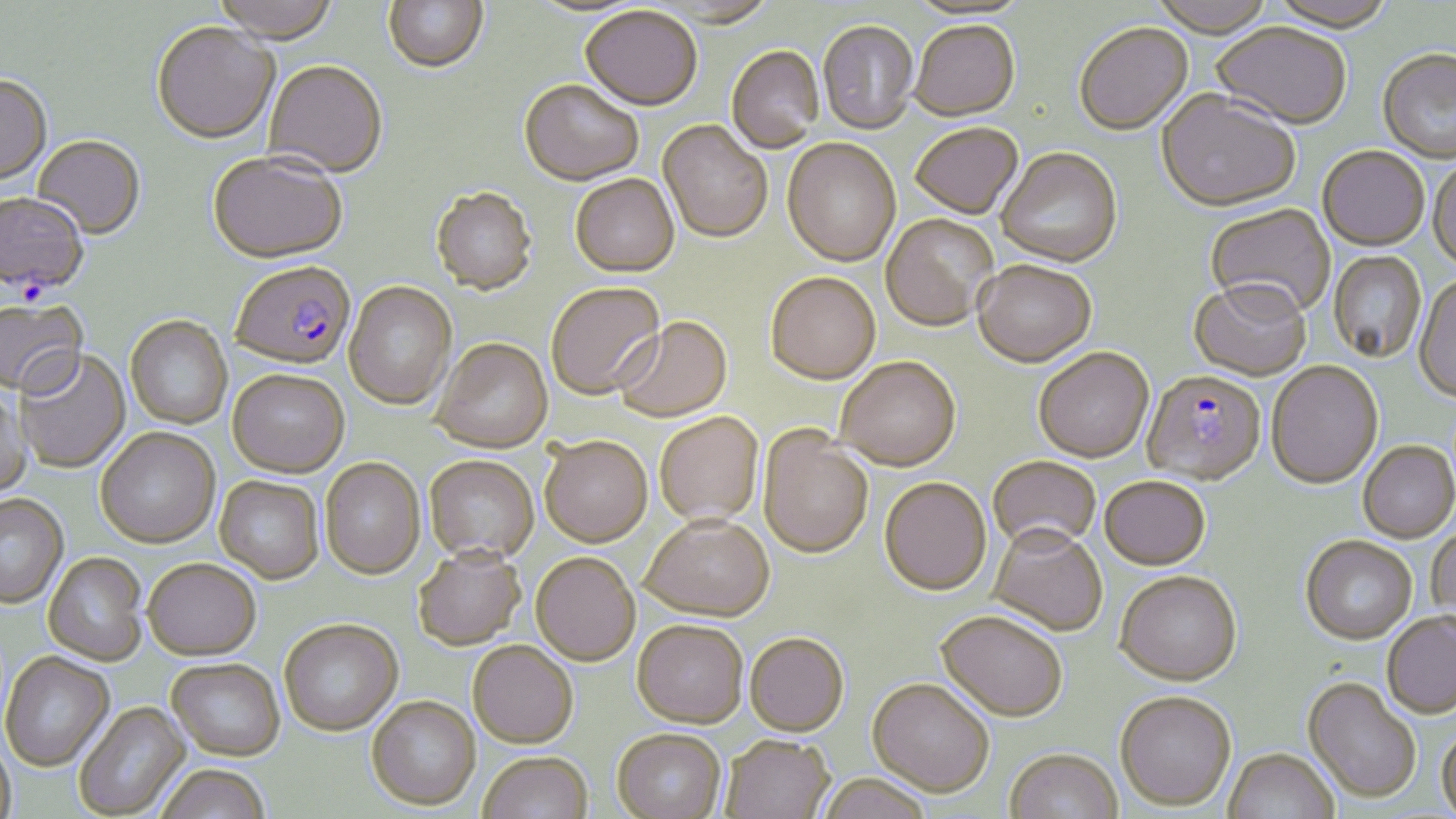

slide-level diagnosis = Plasmodium falciparum
modality = light microscopy
Plasmodium falciparum-infected red blood cell locations = approximate bounding boxes as [x1, y1, x2, y2] in pixels: [0, 194, 89, 298], [229, 263, 355, 374], [1142, 373, 1266, 488]
field of view = single
uninfected red blood cell locations = approximate bounding boxes as [x1, y1, x2, y2] in pixels: [211, 0, 340, 47], [383, 0, 488, 76], [526, 0, 644, 19], [1147, 0, 1277, 41], [1268, 0, 1397, 35], [580, 8, 702, 114], [818, 22, 919, 137], [910, 23, 1020, 124], [151, 24, 279, 148], [1074, 25, 1194, 137], [1211, 25, 1351, 132], [726, 47, 824, 154], [1378, 51, 1456, 165], [263, 63, 387, 180], [0, 77, 53, 188], [519, 81, 643, 189], [1156, 93, 1300, 215], [658, 121, 773, 246], [911, 125, 1023, 221], [32, 137, 145, 241], [782, 140, 900, 268], [1318, 148, 1429, 253], [996, 150, 1123, 270], [208, 155, 348, 267], [1428, 160, 1456, 274], [570, 177, 680, 280], [431, 189, 537, 298], [1205, 204, 1336, 323], [881, 215, 998, 334], [1329, 252, 1426, 364], [972, 264, 1096, 370], [766, 275, 881, 387], [1413, 277, 1456, 405], [343, 282, 457, 411], [1188, 283, 1311, 384], [547, 284, 666, 402], [0, 299, 89, 402], [125, 317, 232, 430], [614, 319, 733, 424], [431, 340, 553, 456], [1034, 349, 1154, 465], [14, 351, 133, 476], [836, 360, 961, 474], [1266, 364, 1383, 492], [227, 372, 349, 481], [0, 388, 33, 499], [655, 414, 764, 528], [757, 429, 873, 561], [95, 430, 220, 551], [539, 439, 653, 550], [1358, 444, 1456, 545], [424, 457, 539, 565], [988, 458, 1100, 557], [320, 460, 425, 582], [214, 477, 324, 586], [880, 480, 991, 598], [1099, 480, 1210, 573], [0, 496, 69, 610], [641, 519, 775, 626], [1427, 526, 1456, 634], [988, 529, 1107, 638], [1300, 538, 1417, 647], [413, 551, 526, 653], [43, 553, 148, 667], [531, 555, 640, 668], [143, 561, 261, 664], [1115, 574, 1242, 690], [935, 614, 1067, 726], [1381, 614, 1456, 721], [279, 622, 403, 738], [632, 624, 748, 731], [745, 636, 849, 739], [468, 643, 577, 751], [1, 653, 115, 772], [166, 660, 285, 764], [1302, 680, 1420, 805], [867, 681, 993, 800], [1115, 695, 1236, 813], [366, 699, 481, 812], [74, 702, 190, 819], [1436, 728, 1456, 818], [612, 732, 726, 819], [0, 736, 16, 819], [720, 738, 835, 819], [1223, 751, 1339, 819], [1005, 752, 1123, 819], [478, 755, 593, 819], [155, 767, 272, 819], [816, 777, 933, 819]
image size = 1456×819 pixels
stain = May-Grünwald-Giemsa
preparation = thin blood smear
magnification = 1000x